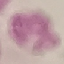

Result: negative for malaria parasites. Giemsa stain. Cell patch, automatically extracted from a larger field of view and resized to 64 × 64 pixels. Photographed with a smartphone camera at the microscope eyepiece. Thin blood film.